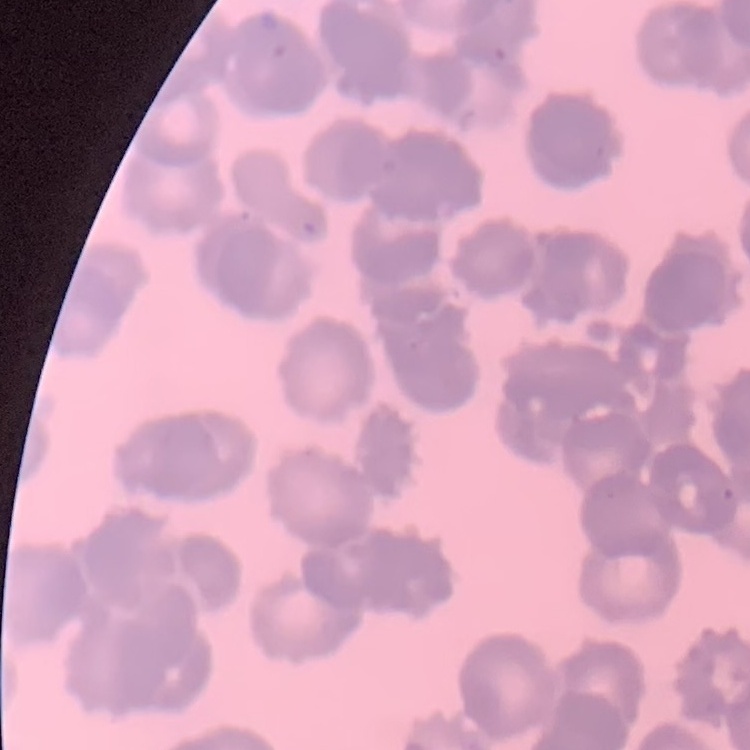
Summary:
  - Red blood cell morphology: rouleaux formation
  - Stain: Field's or Giemsa
  - Image type: one tile cut from a larger photomicrograph
  - Preparation: thin blood smear